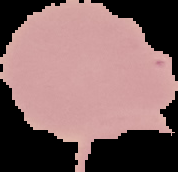

image type = segmented cell region on a black background
preparation = thin blood smear
malaria status = uninfected
image size = 178×172 pixels